Outline each blood parasite and name the species.
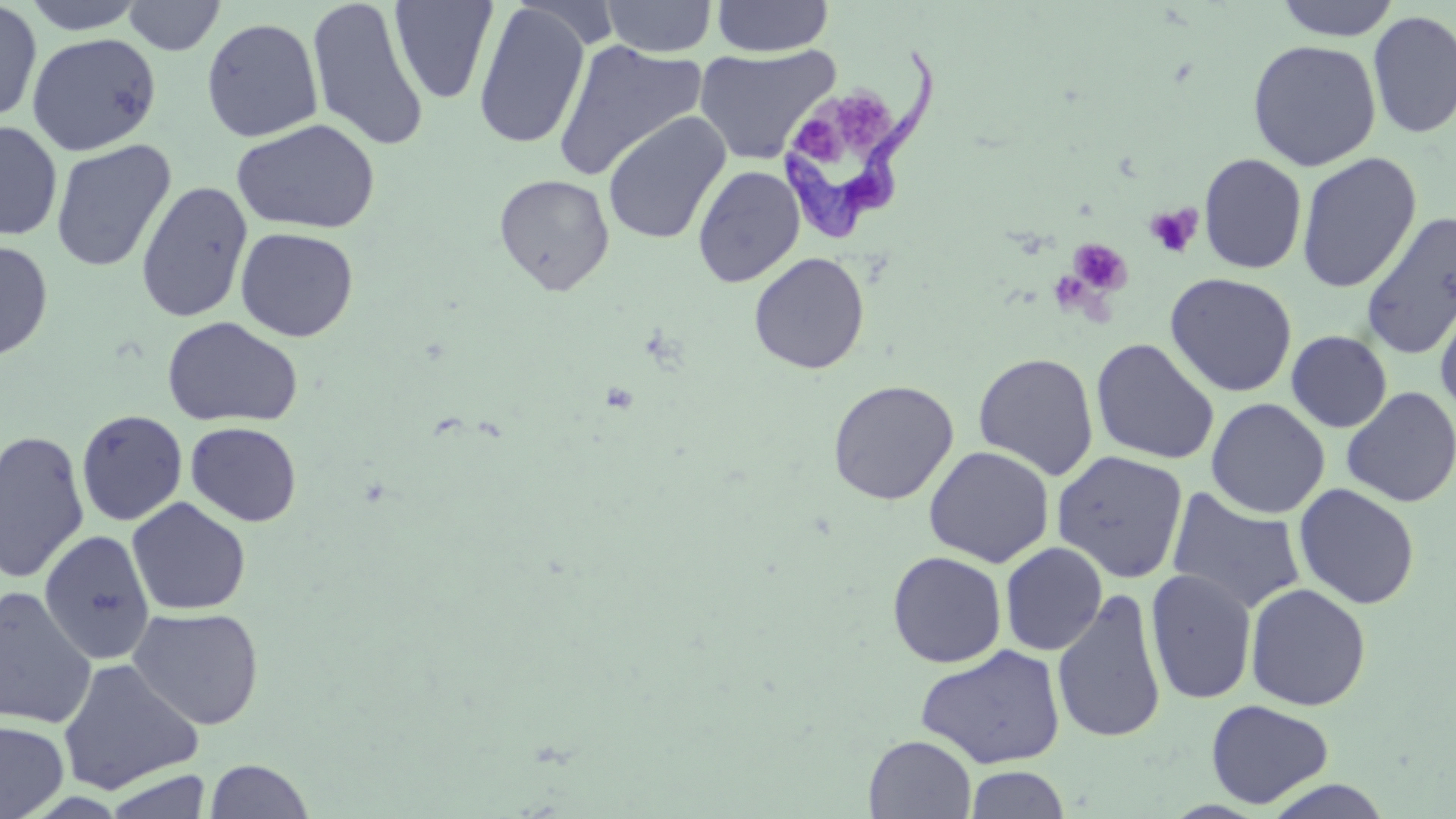

Approximate bounding boxes as (x1,y1)-(x2,y2) corner pairs in pixels.
Trypanosoma brucei: (776,45)-(938,242).
No Plasmodium falciparum, Plasmodium ovale, Plasmodium malariae, Plasmodium vivax, or Babesia divergens observed.

Summary:
  - Uninfected red blood cell locations: (0,0)-(42,124), (21,0)-(149,34), (122,0)-(225,55), (306,0)-(430,153), (601,0)-(718,57), (711,0)-(834,57), (1273,0)-(1402,40), (388,1)-(499,105), (472,3)-(591,150), (1367,9)-(1456,139), (201,17)-(323,143), (26,32)-(161,155), (553,38)-(707,182), (1247,40)-(1382,171), (693,45)-(840,165), (602,111)-(732,245), (231,118)-(381,234), (1,120)-(63,242), (50,139)-(176,272), (1296,152)-(1422,293), (1198,153)-(1307,274), (692,164)-(805,288), (494,174)-(615,295), (136,180)-(253,323), (1359,211)-(1456,361), (235,226)-(359,342), (0,239)-(54,361), (748,252)-(870,374), (1164,272)-(1298,398), (1434,287)-(1456,424), (162,316)-(303,428), (1286,330)-(1392,433), (1090,338)-(1219,465), (973,352)-(1099,480), (827,379)-(959,505), (1341,386)-(1456,508), (1206,398)-(1330,518), (75,409)-(188,526), (185,421)-(302,527), (0,429)-(91,584), (924,445)-(1055,567), (1052,450)-(1189,584), (1294,483)-(1420,610), (1166,487)-(1307,616), (126,497)-(251,616), (39,529)-(156,666), (1000,542)-(1108,656), (887,551)-(1007,668), (1145,568)-(1257,705), (1245,582)-(1371,711), (0,587)-(98,729), (1051,589)-(1168,744), (127,606)-(264,730), (915,644)-(1066,769), (57,657)-(203,795), (1205,699)-(1334,809), (0,720)-(69,819), (863,735)-(977,818), (863,758)-(1069,816), (204,760)-(315,818), (964,765)-(1071,818), (103,769)-(213,819), (1260,779)-(1396,818)
  - Platelet locations: (832,90)-(894,149), (793,114)-(842,169), (1145,203)-(1203,258), (1069,238)-(1132,295)
  - Slide-level diagnosis: Trypanosoma brucei
  - Preparation: thin blood smear
  - Modality: optical microscopy
  - Magnification: 1000x
  - Stain: May-Grünwald-Giemsa
  - Field of view: single
  - Image size: 1456×819 pixels